Report the malaria status of this cell.
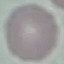
Uninfected.

Acquired by smartphone through the microscope eyepiece. Automatically extracted cell patch, resized to 64 × 64 pixels. Giemsa-stained preparation. Thin smear of blood.